Classify this cell by malaria status.
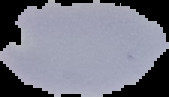

Uninfected.

From a thin blood smear. The area outside the segmented cell region is set to black. Image is 169×97 pixels.